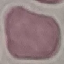

malaria status = uninfected
image type = cell patch, automatically extracted from a larger field of view and resized to 64 × 64 pixels
stain = Giemsa
preparation = thin blood smear
capture = smartphone through the microscope eyepiece